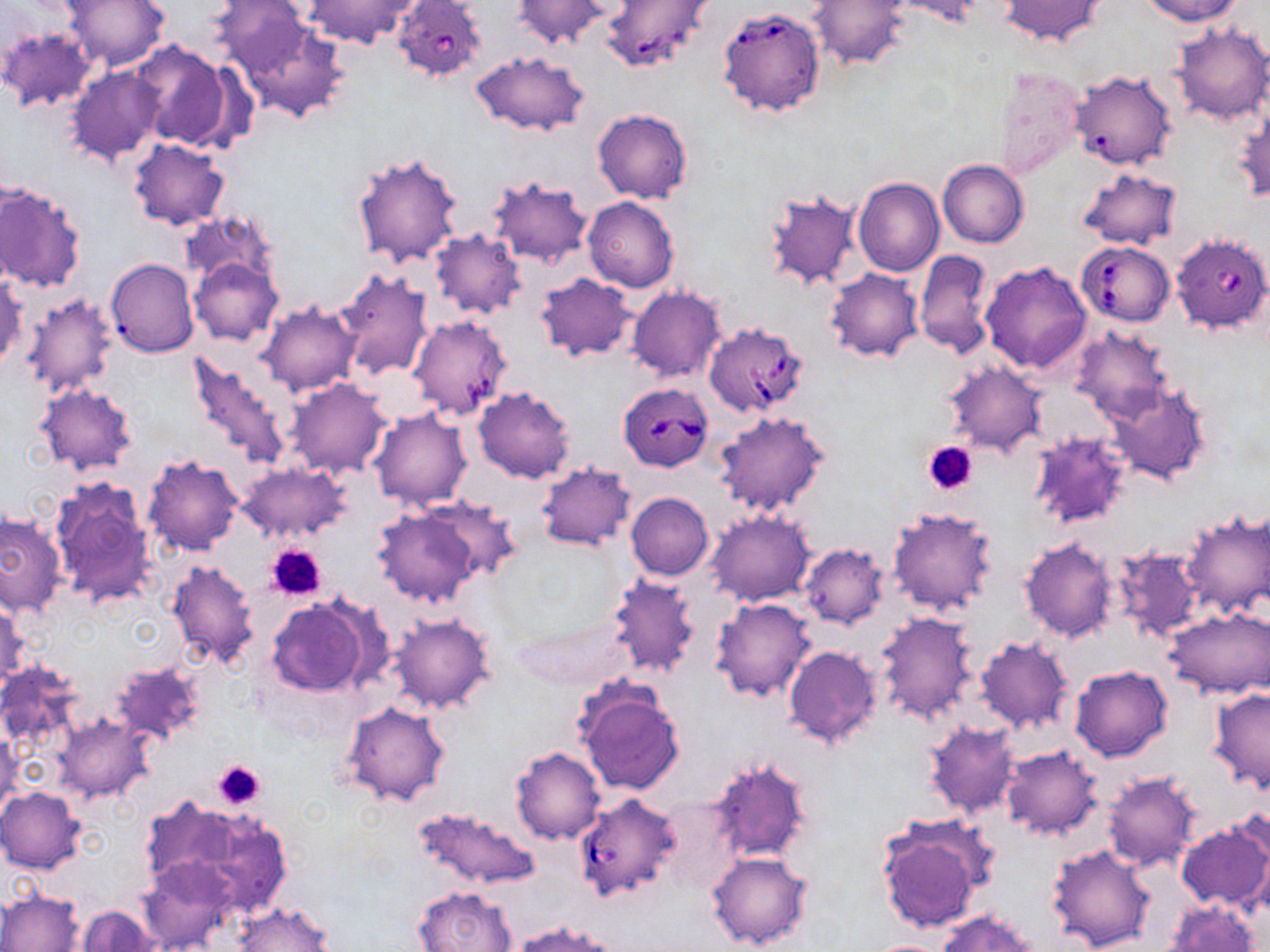
Summary:
  - Coordinate format: approximate bounding boxes as [x1, y1, x2, y2] in pixels
  - Uninfected red blood cell locations: [63, 0, 169, 71], [211, 0, 315, 76], [304, 0, 420, 48], [513, 0, 609, 50], [893, 0, 985, 26], [1002, 0, 1104, 46], [1140, 0, 1242, 24], [809, 1, 909, 70], [235, 13, 351, 123], [1167, 20, 1268, 127], [1, 27, 97, 113], [131, 41, 237, 150], [472, 51, 588, 135], [68, 67, 165, 164], [993, 68, 1085, 179], [1069, 71, 1176, 172], [1234, 104, 1269, 203], [592, 108, 692, 203], [128, 138, 230, 230], [351, 151, 463, 269], [938, 159, 1028, 248], [1077, 166, 1182, 249], [487, 176, 594, 269], [853, 178, 945, 277], [0, 182, 86, 294], [762, 188, 863, 291], [583, 197, 679, 293], [183, 210, 278, 288], [430, 228, 526, 320], [913, 249, 996, 359], [188, 256, 282, 345], [106, 258, 199, 357], [979, 261, 1092, 374], [825, 268, 924, 362], [336, 270, 435, 380], [534, 273, 638, 361], [0, 274, 25, 370], [627, 286, 725, 383], [21, 293, 120, 398], [257, 301, 363, 396], [1068, 326, 1174, 425], [186, 353, 294, 472], [942, 360, 1048, 456], [286, 378, 392, 477], [1108, 382, 1211, 484], [36, 383, 137, 475], [474, 387, 577, 483], [369, 407, 472, 509], [714, 412, 829, 518], [1028, 431, 1134, 530], [141, 455, 245, 557], [236, 461, 353, 545], [535, 464, 637, 551], [49, 476, 156, 608], [626, 493, 713, 580], [423, 497, 522, 584], [372, 506, 483, 607], [887, 506, 1001, 616], [1181, 509, 1269, 618], [706, 510, 815, 606], [0, 513, 66, 617], [1020, 537, 1119, 643], [799, 543, 889, 629], [1107, 547, 1203, 644], [166, 558, 260, 669], [607, 573, 703, 679], [265, 595, 376, 697], [710, 596, 817, 702], [1, 602, 28, 691], [1163, 606, 1269, 698], [874, 612, 981, 724], [390, 614, 494, 714], [975, 637, 1073, 733], [781, 644, 884, 750], [110, 658, 205, 747], [0, 662, 82, 756], [1069, 664, 1172, 762], [573, 679, 686, 796], [1207, 687, 1270, 793], [340, 701, 450, 807], [55, 716, 151, 800], [922, 721, 1020, 820], [0, 732, 21, 820], [1000, 746, 1104, 840], [511, 747, 606, 844], [706, 756, 815, 865], [1101, 771, 1202, 871], [1, 786, 86, 873], [136, 794, 260, 901], [413, 807, 541, 892], [196, 814, 291, 920], [1177, 820, 1270, 912], [878, 821, 989, 932], [1046, 844, 1157, 951], [705, 851, 814, 951], [139, 859, 234, 952], [414, 885, 516, 952], [0, 888, 85, 952], [1161, 898, 1261, 952], [234, 903, 332, 952], [75, 905, 162, 952], [937, 909, 1039, 952], [512, 920, 623, 952], [863, 939, 958, 952]
  - Platelet locations: [924, 441, 977, 495], [265, 544, 328, 601], [213, 759, 267, 810]
  - Babesia divergens-infected red blood cell locations: [393, 0, 487, 79], [601, 0, 716, 73], [717, 7, 825, 118], [1171, 234, 1270, 335], [1077, 242, 1174, 326], [408, 315, 512, 420], [703, 321, 809, 417], [619, 383, 713, 472], [573, 793, 684, 904]
  - Slide-level diagnosis: Babesia divergens
  - Modality: light microscopy
  - Stain: May-Grünwald-Giemsa
  - Image size: 1270×952 pixels
  - Magnification: 1000x
  - Preparation: thin blood smear
  - Field of view: one of a larger specimen